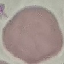

malaria_status: uninfected
preparation: thin blood smear
image_type: cell patch, automatically extracted from a larger field of view and resized to 64 × 64 pixels
stain: Giemsa
capture: smartphone camera at the microscope eyepiece